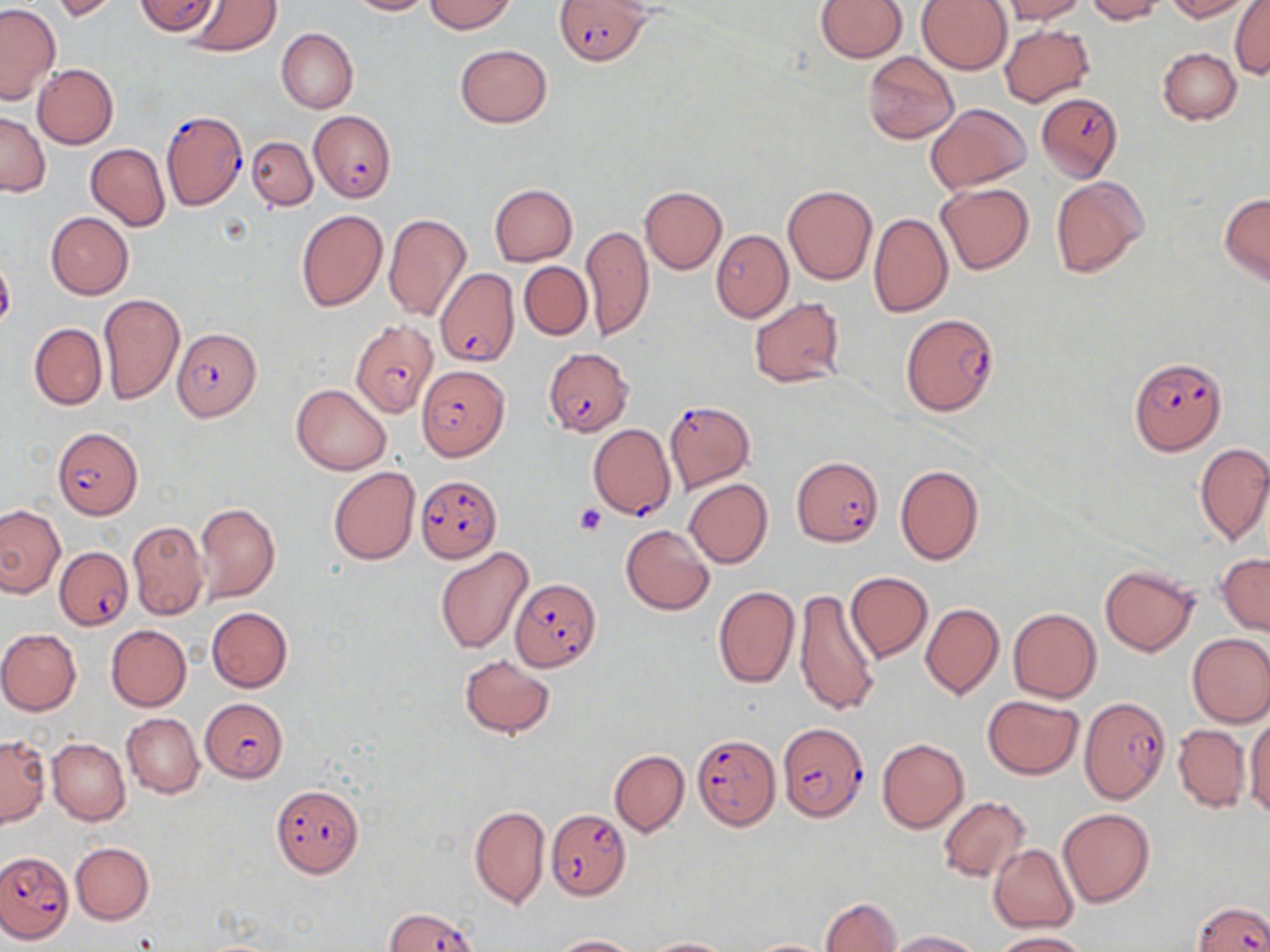

slide-level diagnosis = Plasmodium falciparum
platelet locations = approximate bounding boxes as (x1,y1)-(x2,y2) corner pairs in pixels: (574,504)-(605,535)
modality = light microscopy
Plasmodium falciparum-infected red blood cell locations = approximate bounding boxes as (x1,y1)-(x2,y2) corner pairs in pixels: (554,0)-(650,66), (1036,91)-(1126,182), (161,109)-(248,210), (310,109)-(395,202), (432,263)-(520,373), (901,313)-(998,415), (353,321)-(440,416), (173,327)-(261,423), (541,347)-(632,436), (1128,357)-(1227,455), (416,365)-(508,459), (663,400)-(756,493), (588,424)-(675,520), (52,426)-(142,519), (792,455)-(882,546), (415,475)-(501,562), (55,546)-(132,630), (514,579)-(600,672), (1081,696)-(1172,803), (203,697)-(287,783), (776,722)-(868,821), (691,734)-(779,831), (270,784)-(364,878), (546,808)-(630,900), (2,851)-(73,940), (1194,900)-(1266,951), (386,907)-(478,952)
image size = 1270×952 pixels
uninfected red blood cell locations = approximate bounding boxes as (x1,y1)-(x2,y2) corner pairs in pixels: (50,0)-(122,22), (134,0)-(221,37), (347,0)-(431,16), (425,0)-(515,34), (815,0)-(907,62), (916,0)-(1011,73), (1000,0)-(1086,24), (1085,0)-(1164,23), (1165,0)-(1255,20), (184,1)-(281,56), (1229,1)-(1269,78), (0,4)-(60,102), (999,25)-(1094,106), (277,28)-(358,113), (454,44)-(553,127), (1158,47)-(1241,124), (862,51)-(958,144), (33,64)-(118,149), (925,103)-(1031,193), (0,111)-(50,196), (248,136)-(317,211), (86,144)-(170,230), (1050,176)-(1148,278), (936,181)-(1033,274), (489,185)-(578,265), (783,185)-(877,284), (639,186)-(728,274), (1219,193)-(1270,285), (295,209)-(388,311), (46,212)-(135,299), (869,212)-(953,317), (383,213)-(471,322), (581,224)-(653,342), (710,229)-(792,322), (519,261)-(592,340), (99,293)-(184,404), (748,297)-(846,389), (29,323)-(107,409), (291,384)-(392,475), (1195,444)-(1270,545), (895,464)-(985,565), (328,466)-(420,564), (684,478)-(773,567), (194,502)-(281,603), (0,504)-(65,596), (128,520)-(209,619), (621,525)-(715,615), (435,546)-(536,653), (1217,554)-(1270,635), (1099,564)-(1199,656), (845,572)-(932,662), (713,586)-(800,689), (794,589)-(882,716), (920,603)-(1003,699), (207,607)-(292,691), (1008,608)-(1101,702), (106,624)-(191,711), (0,628)-(82,715), (1187,632)-(1270,728), (459,654)-(556,738), (983,695)-(1085,778), (121,713)-(203,798), (1244,714)-(1270,817), (1173,724)-(1251,813), (0,735)-(49,826), (47,738)-(130,825), (878,739)-(969,833), (610,750)-(689,836), (938,795)-(1031,882), (469,805)-(550,909), (1057,808)-(1155,909), (71,843)-(154,925), (989,844)-(1077,933), (820,897)-(901,952), (885,929)-(982,951), (991,931)-(1090,952), (548,935)-(641,952), (642,937)-(737,951), (748,938)-(833,951)
field of view = single
stain = May-Grünwald-Giemsa
preparation = thin blood smear
magnification = 1000x